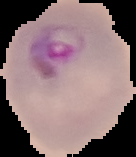
Result: Plasmodium parasites identified. Segmented cell region on a black background. From a thin blood film. Image is 136×157 pixels.